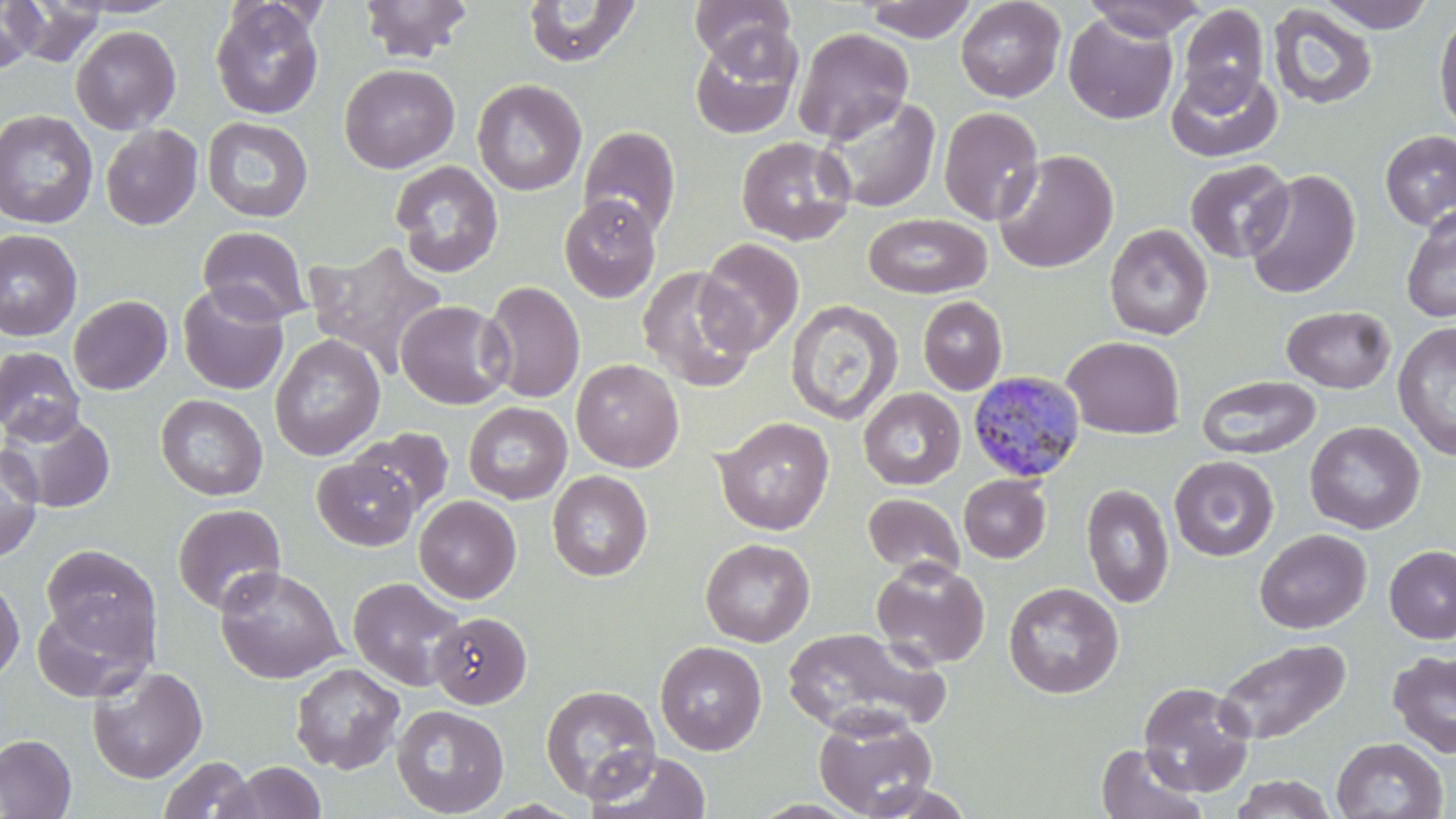
Summary:
  - Coordinate format: approximate bounding boxes as named x1/y1/x2/y2 corners in pixels
  - Plasmodium malariae-infected red blood cell locations: (x1=967, y1=371, x2=1086, y2=484)
  - Uninfected red blood cell locations: (x1=357, y1=0, x2=474, y2=62), (x1=689, y1=0, x2=797, y2=67), (x1=956, y1=0, x2=1066, y2=102), (x1=1082, y1=0, x2=1208, y2=40), (x1=1317, y1=0, x2=1437, y2=32), (x1=0, y1=1, x2=43, y2=75), (x1=4, y1=1, x2=109, y2=68), (x1=522, y1=1, x2=642, y2=68), (x1=862, y1=1, x2=977, y2=42), (x1=209, y1=2, x2=325, y2=120), (x1=1177, y1=4, x2=1269, y2=108), (x1=1267, y1=4, x2=1378, y2=111), (x1=955, y1=5, x2=1177, y2=110), (x1=1433, y1=9, x2=1456, y2=139), (x1=1063, y1=12, x2=1178, y2=125), (x1=70, y1=25, x2=181, y2=134), (x1=689, y1=26, x2=803, y2=140), (x1=793, y1=27, x2=914, y2=145), (x1=339, y1=63, x2=459, y2=173), (x1=1167, y1=64, x2=1282, y2=163), (x1=472, y1=79, x2=587, y2=195), (x1=817, y1=94, x2=942, y2=214), (x1=938, y1=106, x2=1044, y2=225), (x1=0, y1=110, x2=98, y2=229), (x1=202, y1=117, x2=313, y2=223), (x1=100, y1=124, x2=203, y2=230), (x1=578, y1=125, x2=681, y2=238), (x1=1380, y1=130, x2=1456, y2=229), (x1=736, y1=136, x2=856, y2=245), (x1=993, y1=149, x2=1119, y2=274), (x1=1184, y1=159, x2=1294, y2=264), (x1=389, y1=160, x2=504, y2=278), (x1=1243, y1=169, x2=1360, y2=298), (x1=559, y1=194, x2=661, y2=302), (x1=1401, y1=204, x2=1456, y2=323), (x1=863, y1=213, x2=992, y2=298), (x1=1104, y1=223, x2=1214, y2=340), (x1=197, y1=226, x2=311, y2=325), (x1=0, y1=229, x2=83, y2=342), (x1=695, y1=238, x2=804, y2=356), (x1=303, y1=240, x2=448, y2=376), (x1=636, y1=266, x2=758, y2=393), (x1=481, y1=280, x2=585, y2=403), (x1=177, y1=284, x2=289, y2=395), (x1=68, y1=295, x2=172, y2=395), (x1=917, y1=296, x2=1007, y2=395), (x1=785, y1=298, x2=903, y2=426), (x1=395, y1=300, x2=512, y2=409), (x1=1282, y1=305, x2=1396, y2=393), (x1=1392, y1=321, x2=1456, y2=461), (x1=269, y1=334, x2=385, y2=460), (x1=1062, y1=336, x2=1185, y2=438), (x1=0, y1=346, x2=85, y2=444), (x1=571, y1=359, x2=684, y2=472), (x1=1197, y1=375, x2=1321, y2=460), (x1=858, y1=387, x2=965, y2=490), (x1=155, y1=394, x2=268, y2=500), (x1=463, y1=402, x2=572, y2=504), (x1=2, y1=410, x2=115, y2=514), (x1=713, y1=416, x2=834, y2=535), (x1=1304, y1=420, x2=1425, y2=535), (x1=349, y1=428, x2=454, y2=517), (x1=0, y1=444, x2=44, y2=563), (x1=1169, y1=455, x2=1278, y2=561), (x1=312, y1=457, x2=419, y2=550), (x1=547, y1=471, x2=653, y2=581), (x1=958, y1=474, x2=1050, y2=563), (x1=1081, y1=483, x2=1174, y2=608), (x1=862, y1=493, x2=964, y2=579), (x1=414, y1=495, x2=521, y2=603), (x1=172, y1=503, x2=287, y2=615), (x1=1254, y1=528, x2=1372, y2=634), (x1=700, y1=537, x2=815, y2=647), (x1=40, y1=543, x2=161, y2=659), (x1=1385, y1=545, x2=1456, y2=644), (x1=871, y1=559, x2=990, y2=669), (x1=215, y1=566, x2=346, y2=685), (x1=0, y1=574, x2=25, y2=686), (x1=348, y1=577, x2=466, y2=691), (x1=1003, y1=582, x2=1124, y2=699), (x1=32, y1=599, x2=154, y2=702), (x1=429, y1=611, x2=532, y2=709), (x1=781, y1=626, x2=949, y2=737), (x1=1213, y1=638, x2=1351, y2=745), (x1=655, y1=640, x2=767, y2=755), (x1=1388, y1=650, x2=1456, y2=759), (x1=290, y1=662, x2=405, y2=773), (x1=87, y1=664, x2=208, y2=783), (x1=1138, y1=681, x2=1256, y2=797), (x1=540, y1=684, x2=661, y2=803), (x1=392, y1=704, x2=509, y2=817), (x1=813, y1=708, x2=939, y2=819), (x1=0, y1=733, x2=77, y2=818), (x1=1331, y1=736, x2=1448, y2=819), (x1=1095, y1=744, x2=1207, y2=819), (x1=583, y1=750, x2=713, y2=819), (x1=158, y1=756, x2=255, y2=819), (x1=225, y1=761, x2=327, y2=818), (x1=1229, y1=774, x2=1338, y2=818), (x1=856, y1=782, x2=978, y2=818)
  - Slide-level diagnosis: Plasmodium malariae
  - Image size: 1456×819 pixels
  - Magnification: 1000x
  - Preparation: thin blood smear
  - Modality: light microscopy
  - Stain: May-Grünwald-Giemsa
  - Field of view: one of a larger specimen